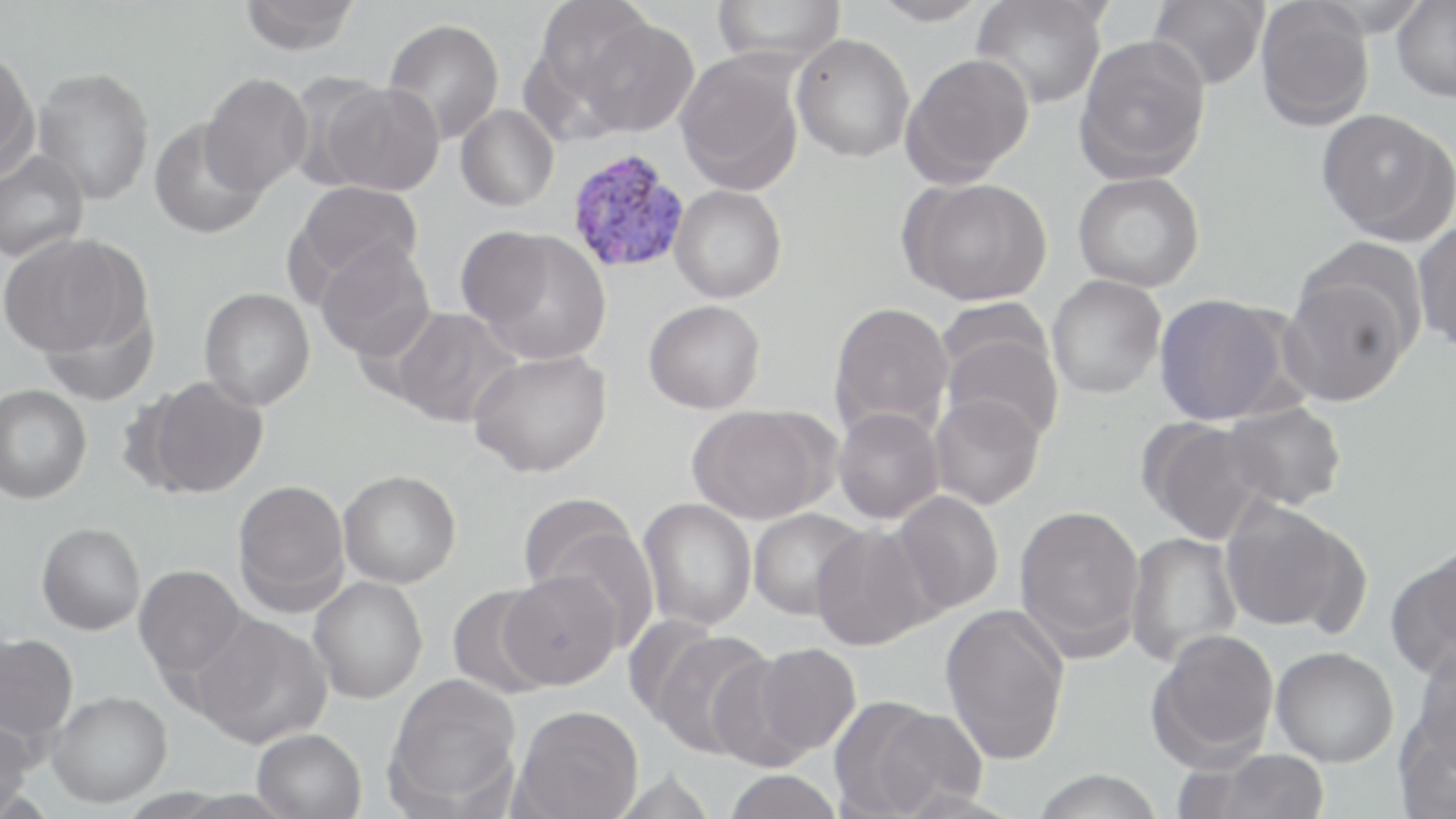
Summary:
  - Coordinate format: approximate bounding boxes as [x1, y1, x2, y2] in pixels
  - Uninfected red blood cell locations: [238, 0, 361, 54], [536, 0, 656, 100], [711, 0, 846, 67], [869, 0, 991, 26], [971, 0, 1109, 109], [1392, 0, 1456, 102], [1148, 1, 1268, 90], [1255, 1, 1374, 131], [382, 18, 505, 144], [577, 18, 698, 137], [791, 33, 915, 162], [1074, 34, 1211, 184], [518, 44, 626, 148], [0, 47, 40, 179], [675, 51, 805, 195], [901, 53, 1035, 187], [32, 66, 155, 205], [199, 72, 313, 195], [317, 81, 445, 196], [455, 105, 558, 211], [1316, 108, 1454, 245], [148, 120, 267, 240], [0, 150, 89, 262], [1073, 171, 1205, 292], [898, 176, 1053, 306], [288, 182, 423, 295], [669, 184, 787, 303], [1413, 221, 1456, 352], [467, 229, 613, 364], [1, 233, 144, 359], [315, 239, 436, 362], [1279, 269, 1415, 407], [1046, 276, 1166, 399], [199, 288, 315, 410], [1154, 294, 1294, 426], [39, 298, 159, 406], [643, 299, 766, 413], [828, 302, 954, 441], [388, 307, 520, 427], [940, 320, 1064, 445], [468, 348, 612, 477], [136, 375, 269, 498], [0, 384, 92, 504], [928, 392, 1045, 510], [1221, 401, 1347, 511], [687, 404, 836, 524], [832, 407, 945, 524], [1139, 417, 1276, 544], [338, 469, 461, 588], [232, 479, 350, 614], [891, 490, 1004, 615], [638, 498, 757, 631], [1220, 499, 1360, 634], [1014, 504, 1146, 660], [748, 508, 867, 620], [528, 512, 660, 647], [36, 522, 145, 634], [811, 523, 938, 651], [1125, 532, 1242, 667], [1385, 545, 1456, 680], [134, 565, 247, 680], [498, 570, 622, 691], [309, 576, 428, 704], [446, 585, 557, 699], [940, 604, 1071, 765], [187, 613, 332, 748], [644, 628, 775, 761], [1146, 629, 1281, 768], [0, 632, 78, 744], [748, 643, 861, 756], [1408, 644, 1456, 777], [1271, 646, 1399, 767], [705, 650, 823, 770], [385, 674, 522, 812], [46, 691, 172, 808], [830, 697, 973, 818], [1394, 702, 1456, 819], [512, 705, 643, 819], [0, 714, 34, 819], [252, 728, 366, 819], [1191, 748, 1331, 819], [1031, 768, 1165, 819], [607, 770, 718, 818], [723, 770, 844, 819]
  - Plasmodium vivax-infected red blood cell locations: [565, 149, 691, 275]
  - Slide-level diagnosis: Plasmodium vivax
  - Image size: 1456×819 pixels
  - Field of view: one of a larger specimen
  - Magnification: 1000x
  - Preparation: thin blood smear
  - Stain: May-Grünwald-Giemsa
  - Modality: light microscopy